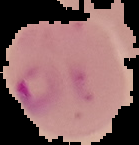 Malaria status: parasitized. From a thin blood smear. Cell region segmented out of the field of view; the surrounding area is masked to black. Image is 139×145 pixels.